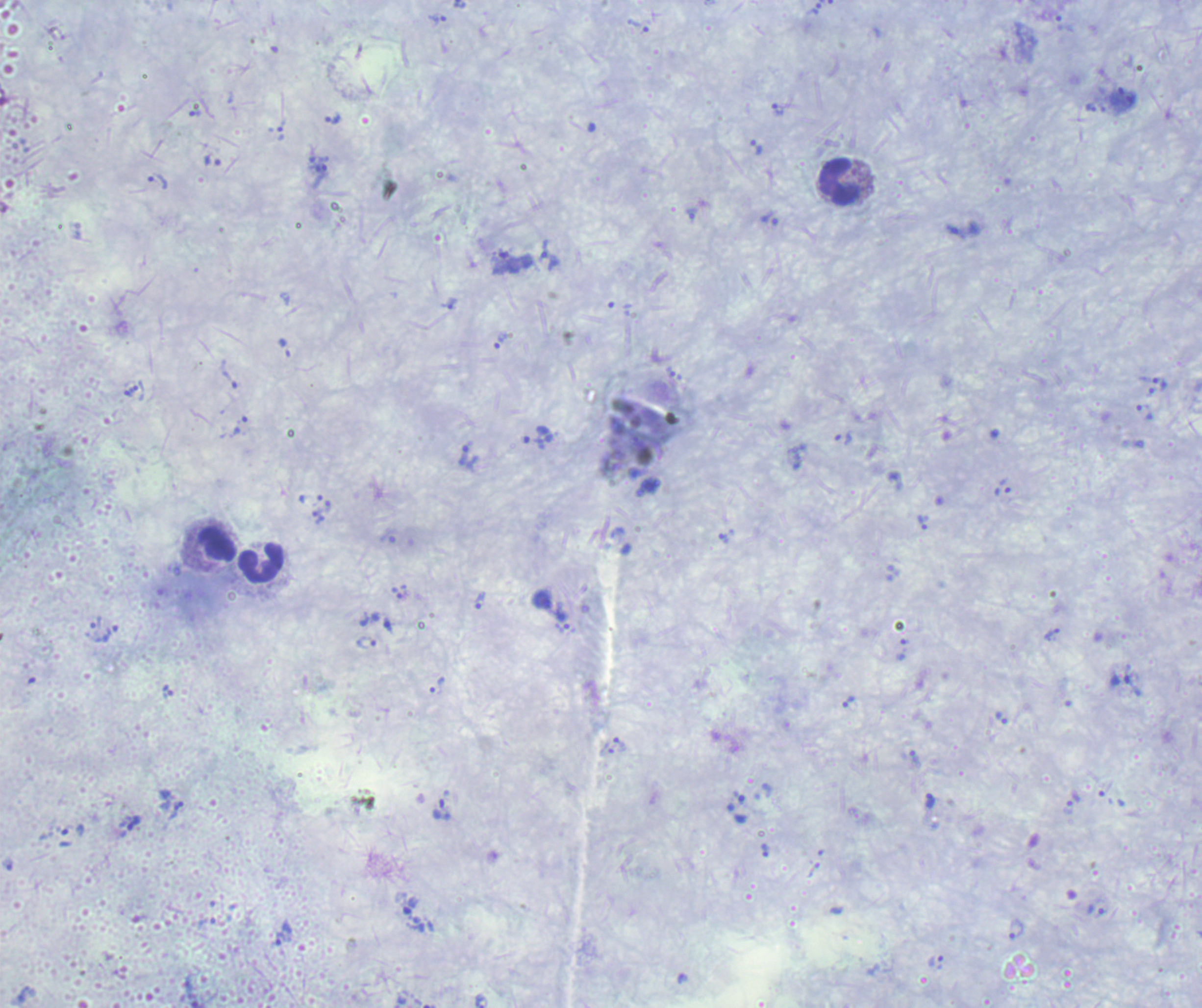
Approximate object centers, in pixels from the top-left corner. Leukocyte locations: (x=839, y=182), (x=217, y=543), (x=262, y=564). Trophozoite locations: (x=814, y=8), (x=437, y=19), (x=1090, y=106), (x=778, y=109), (x=196, y=113), (x=333, y=119), (x=280, y=133), (x=757, y=148), (x=321, y=168), (x=158, y=182), (x=769, y=218), (x=550, y=261), (x=449, y=303), (x=501, y=340), (x=1160, y=384), (x=134, y=389), (x=1144, y=411), (x=240, y=426), (x=843, y=438), (x=464, y=455), (x=1002, y=491), (x=318, y=518), (x=922, y=522), (x=724, y=537), (x=481, y=601), (x=390, y=626), (x=110, y=633), (x=1051, y=636), (x=1120, y=680), (x=437, y=686), (x=168, y=692), (x=849, y=701), (x=1001, y=718), (x=930, y=800), (x=1068, y=808), (x=134, y=824), (x=73, y=830), (x=765, y=850), (x=1095, y=911), (x=1017, y=929), (x=280, y=938). Background quality: poor. Image is 1202×1008 pixels. Romanowsky stain. Single field of view. Previously used in an actual diagnosis. Thick smear of blood. Result: positive for Plasmodium parasites. Captured at 100x magnification.